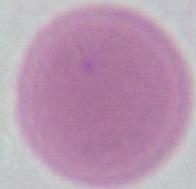
1000x magnification. Photomicrograph. An erythrocyte is shown.